Report the malaria status of this cell.
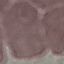
It is uninfected.

Summary:
  - Preparation: thin smear
  - Stain: Giemsa
  - Capture: smartphone camera at the microscope eyepiece
  - Image type: automatically extracted cell patch, resized to 64 × 64 pixels